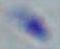

identification = Toxoplasma gondii
magnification = 1000x
modality = micrograph